Give the extent of all Plasmodium vivax-infected red blood cells.
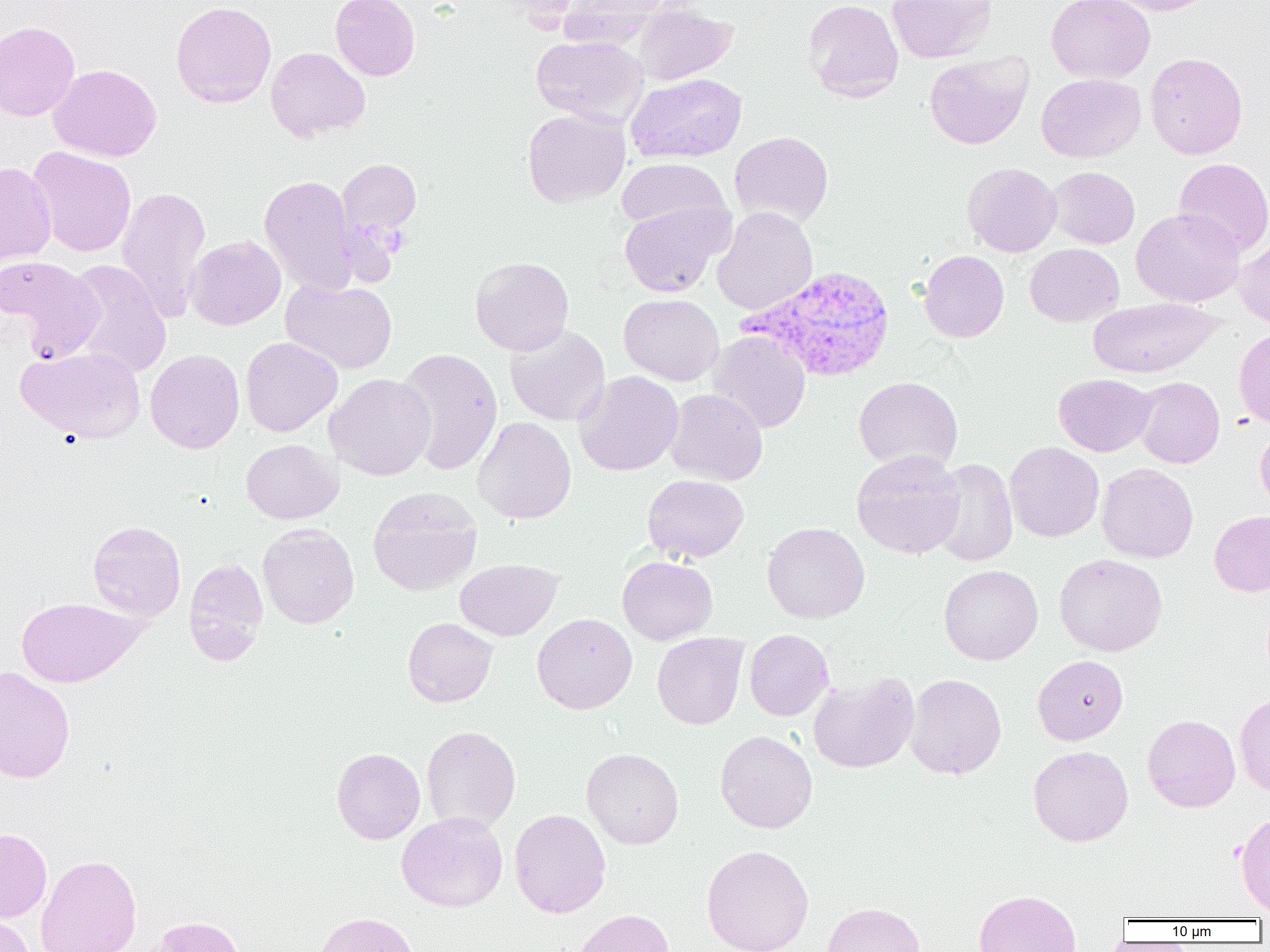

Approximate bounding boxes as named x1/y1/x2/y2 corners in pixels.
Plasmodium vivax-infected red blood cells: (x1=741, y1=265, x2=897, y2=383).

{
  "slide_level_diagnosis": "Plasmodium vivax",
  "modality": "optical microscopy",
  "magnification": "1000x",
  "uninfected_red_blood_cell_locations": "approximate bounding boxes as named x1/y1/x2/y2 corners in pixels: (x1=330, y1=0, x2=420, y2=81), (x1=803, y1=0, x2=904, y2=103), (x1=887, y1=0, x2=999, y2=63), (x1=1046, y1=0, x2=1155, y2=83), (x1=1104, y1=0, x2=1218, y2=15), (x1=171, y1=1, x2=277, y2=108), (x1=558, y1=1, x2=669, y2=48), (x1=632, y1=3, x2=738, y2=85), (x1=0, y1=21, x2=80, y2=121), (x1=531, y1=35, x2=647, y2=126), (x1=266, y1=47, x2=370, y2=142), (x1=924, y1=52, x2=1033, y2=150), (x1=1145, y1=52, x2=1248, y2=159), (x1=48, y1=64, x2=162, y2=162), (x1=626, y1=73, x2=747, y2=163), (x1=1036, y1=73, x2=1146, y2=163), (x1=522, y1=109, x2=630, y2=208), (x1=730, y1=131, x2=834, y2=226), (x1=28, y1=146, x2=137, y2=257), (x1=335, y1=156, x2=422, y2=257), (x1=616, y1=158, x2=730, y2=232), (x1=1173, y1=158, x2=1270, y2=257), (x1=0, y1=162, x2=56, y2=269), (x1=962, y1=163, x2=1061, y2=256), (x1=1048, y1=167, x2=1139, y2=248), (x1=260, y1=174, x2=359, y2=295), (x1=116, y1=185, x2=211, y2=323), (x1=620, y1=201, x2=731, y2=297), (x1=712, y1=206, x2=818, y2=316), (x1=1131, y1=208, x2=1245, y2=307), (x1=186, y1=235, x2=286, y2=330), (x1=1234, y1=237, x2=1270, y2=329), (x1=1025, y1=243, x2=1124, y2=326), (x1=918, y1=250, x2=1009, y2=342), (x1=1, y1=255, x2=103, y2=358), (x1=470, y1=256, x2=574, y2=356), (x1=62, y1=260, x2=172, y2=378), (x1=281, y1=279, x2=397, y2=374), (x1=618, y1=294, x2=724, y2=385), (x1=1088, y1=297, x2=1221, y2=379), (x1=505, y1=325, x2=610, y2=426), (x1=1233, y1=326, x2=1270, y2=429), (x1=708, y1=331, x2=810, y2=433), (x1=240, y1=337, x2=342, y2=437), (x1=17, y1=346, x2=145, y2=444), (x1=396, y1=348, x2=503, y2=476), (x1=145, y1=349, x2=244, y2=454), (x1=686, y1=354, x2=788, y2=470), (x1=574, y1=371, x2=683, y2=476), (x1=325, y1=373, x2=436, y2=480), (x1=1054, y1=374, x2=1155, y2=456), (x1=853, y1=376, x2=963, y2=473), (x1=1134, y1=377, x2=1224, y2=468), (x1=664, y1=388, x2=768, y2=485), (x1=473, y1=416, x2=576, y2=524), (x1=1255, y1=424, x2=1270, y2=517), (x1=241, y1=438, x2=343, y2=524), (x1=1005, y1=442, x2=1104, y2=542), (x1=851, y1=449, x2=965, y2=559), (x1=929, y1=458, x2=1018, y2=567), (x1=1096, y1=463, x2=1198, y2=563), (x1=643, y1=474, x2=749, y2=563), (x1=368, y1=486, x2=483, y2=596), (x1=1209, y1=510, x2=1270, y2=596), (x1=88, y1=520, x2=186, y2=621), (x1=762, y1=522, x2=870, y2=624), (x1=258, y1=523, x2=359, y2=628), (x1=1054, y1=553, x2=1167, y2=657), (x1=617, y1=556, x2=717, y2=645), (x1=183, y1=558, x2=269, y2=665), (x1=455, y1=559, x2=562, y2=641), (x1=939, y1=564, x2=1043, y2=665), (x1=16, y1=597, x2=144, y2=688), (x1=532, y1=614, x2=637, y2=714), (x1=403, y1=617, x2=498, y2=707), (x1=744, y1=629, x2=834, y2=721), (x1=652, y1=633, x2=748, y2=730), (x1=1033, y1=654, x2=1128, y2=745), (x1=0, y1=666, x2=75, y2=784), (x1=808, y1=671, x2=918, y2=773), (x1=905, y1=674, x2=1006, y2=779), (x1=1234, y1=693, x2=1270, y2=796), (x1=1142, y1=714, x2=1241, y2=812), (x1=421, y1=726, x2=521, y2=833), (x1=715, y1=730, x2=817, y2=833), (x1=1028, y1=745, x2=1133, y2=846), (x1=332, y1=747, x2=425, y2=844), (x1=582, y1=748, x2=683, y2=849), (x1=510, y1=809, x2=611, y2=918), (x1=1235, y1=811, x2=1270, y2=916), (x1=397, y1=812, x2=507, y2=912), (x1=0, y1=828, x2=51, y2=923), (x1=701, y1=845, x2=814, y2=952), (x1=35, y1=853, x2=142, y2=952), (x1=973, y1=889, x2=1082, y2=952), (x1=820, y1=902, x2=925, y2=952), (x1=570, y1=909, x2=675, y2=952), (x1=313, y1=912, x2=420, y2=952), (x1=0, y1=914, x2=36, y2=952), (x1=144, y1=916, x2=247, y2=952)",
  "preparation": "thin blood film",
  "image_size": "1270×952 pixels",
  "field_of_view": "single"
}